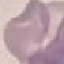
Malaria status: uninfected. Giemsa stain. Thin blood smear. Cell patch, automatically extracted from a larger field of view and resized to 64 × 64 pixels. Acquired by smartphone through the microscope eyepiece.